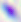
magnification = 400x
identification = Toxoplasma gondii
modality = micrograph